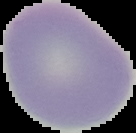

Summary:
  - Preparation: thin blood smear
  - Image size: 136×133 pixels
  - Image type: segmented cell region with the area outside set to black
  - Malaria status: uninfected